Classify this cell by malaria status.
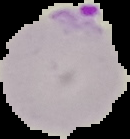

Parasitized.

Summary:
  - Preparation: thin blood film
  - Image size: 130×139 pixels
  - Image type: segmented cell region on a black background